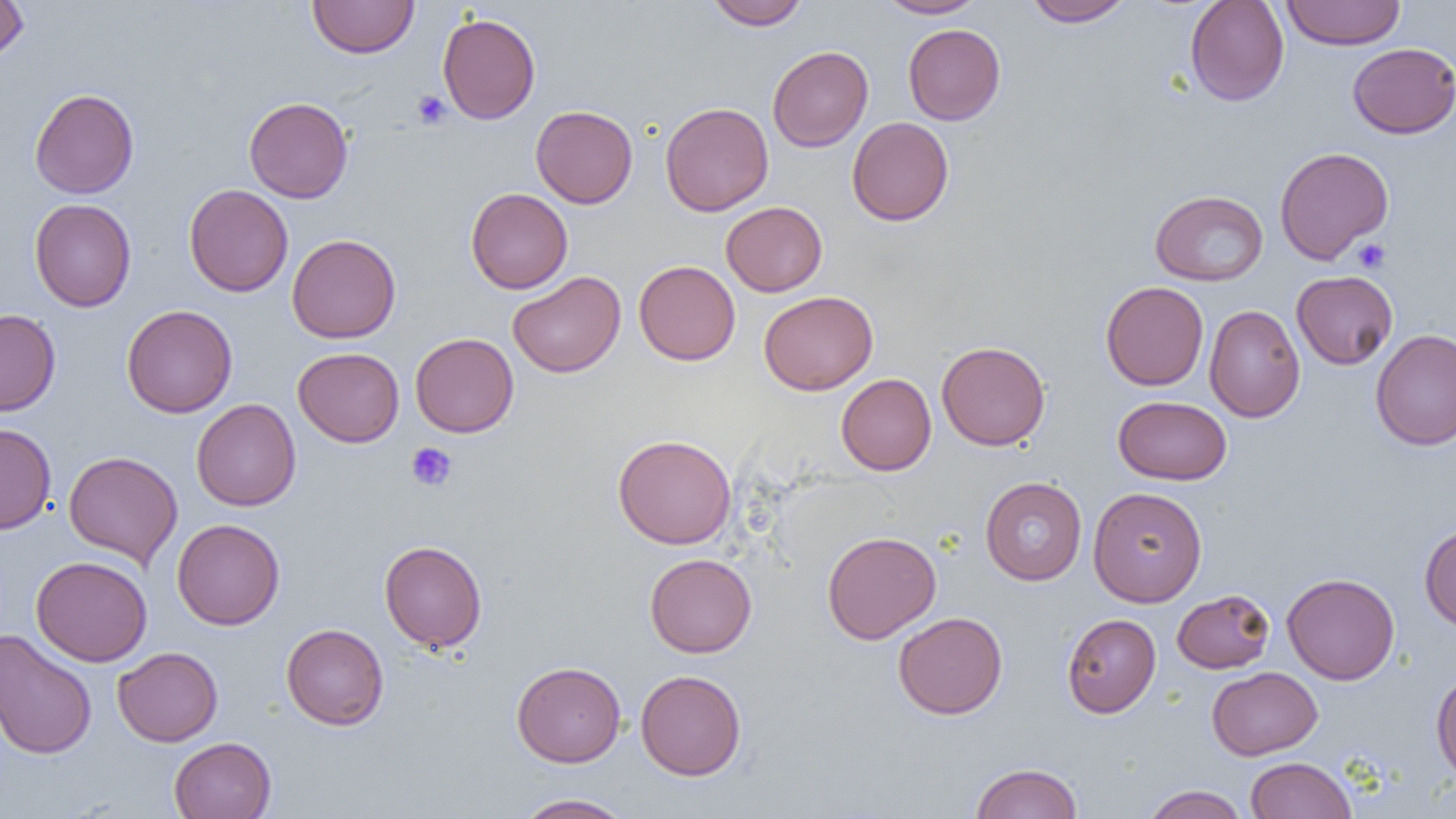
Approximate bounding boxes as [x1, y1, x2, y2] in pixels. Platelet locations: [411, 90, 452, 129], [1352, 238, 1391, 273], [406, 442, 457, 491]. Uninfected red blood cell locations: [0, 0, 29, 62], [307, 0, 419, 58], [706, 0, 809, 31], [876, 0, 987, 18], [1023, 0, 1134, 27], [1185, 0, 1289, 106], [1281, 0, 1405, 49], [437, 13, 541, 124], [903, 24, 1006, 125], [1347, 42, 1456, 138], [767, 46, 873, 151], [29, 88, 139, 199], [244, 97, 353, 203], [660, 102, 774, 216], [530, 105, 638, 208], [847, 117, 954, 226], [1274, 146, 1393, 264], [184, 184, 293, 297], [466, 188, 573, 293], [1150, 190, 1268, 286], [29, 199, 137, 312], [721, 201, 828, 296], [287, 233, 401, 343], [634, 260, 740, 365], [507, 271, 626, 378], [1292, 271, 1398, 369], [1101, 281, 1209, 391], [759, 290, 878, 395], [121, 304, 237, 418], [1205, 305, 1305, 422], [0, 309, 61, 415], [1370, 329, 1456, 450], [410, 332, 519, 437], [936, 340, 1051, 450], [293, 347, 404, 447], [836, 374, 936, 475], [1113, 395, 1231, 485], [191, 399, 301, 511], [0, 423, 56, 535], [612, 433, 737, 549], [64, 451, 183, 568], [980, 477, 1086, 585], [1088, 486, 1207, 607], [172, 518, 285, 630], [1419, 524, 1456, 631], [822, 531, 941, 644], [379, 540, 487, 652], [645, 553, 757, 657], [31, 555, 152, 666], [1282, 573, 1399, 684], [1172, 589, 1275, 673], [893, 612, 1008, 719], [1062, 613, 1161, 718], [281, 623, 389, 730], [1, 630, 97, 761], [113, 646, 223, 747], [512, 661, 626, 767], [1207, 666, 1322, 760], [635, 669, 747, 780], [1431, 669, 1456, 783], [169, 737, 277, 819], [1245, 757, 1356, 819], [969, 762, 1083, 819], [1142, 785, 1249, 819], [513, 793, 634, 819]. Slide-level diagnosis: no evidence of blood parasites. Optical microscopy. Captured at 1000x magnification. Image is 1456×819 pixels. Single field of view. Thin blood film.